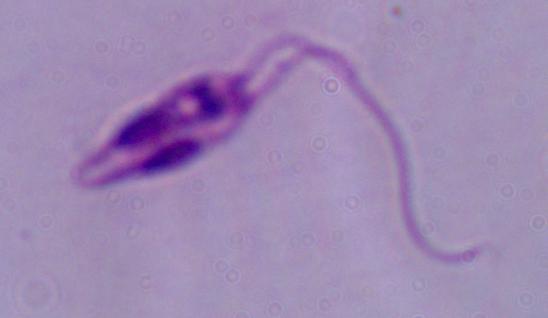

Summary:
  - Magnification: 1000x
  - Identification: Leishmania
  - Modality: photomicrograph